Name the cell type shown.
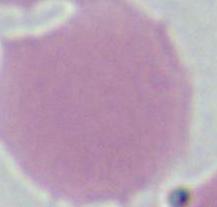

This is an erythrocyte.

1000x magnification. Photomicrograph.